Classify this cell by malaria status.
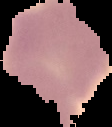
It is uninfected.

preparation = thin blood film
image type = segmented cell region on a black background
image size = 112×127 pixels